Locate malaria parasites and leukocytes.
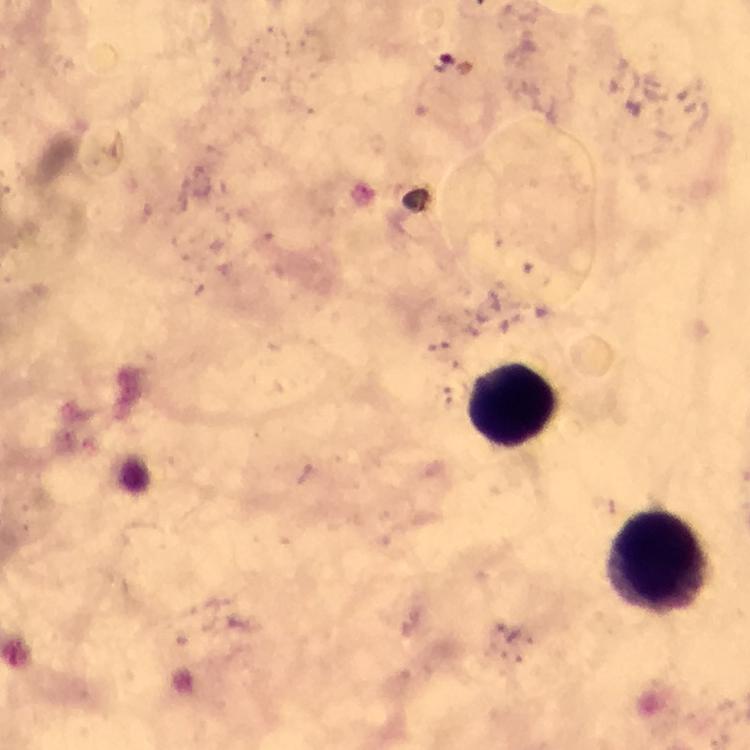
No malaria parasites seen.
Approximate object centers, in pixels from the top-left corner.
Leukocytes: (x=515, y=402), (x=658, y=563).

Summary:
  - Context: from a malaria diagnostic workup
  - Immersion oil: applied
  - Preparation: thick blood smear
  - Cropped from: a single field of view
  - Magnification: 100x
  - Image size: 750×750 pixels
  - Stain: Giemsa
  - Capture: smartphone photograph through a microscope